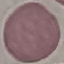

Malaria status: uninfected. Thin blood film. Cell patch, automatically extracted from a larger field of view and resized to 64 × 64 pixels. Acquired by smartphone through the microscope eyepiece. Giemsa stain.